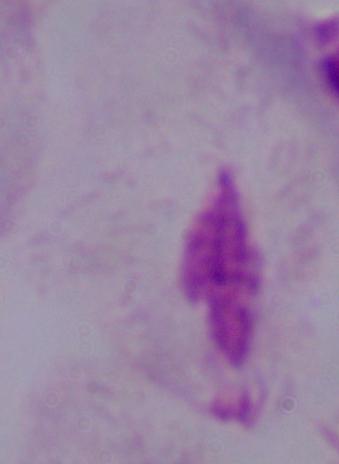
magnification = 1000x
identification = trichomonad
modality = photomicrograph